Name the blood parasite species.
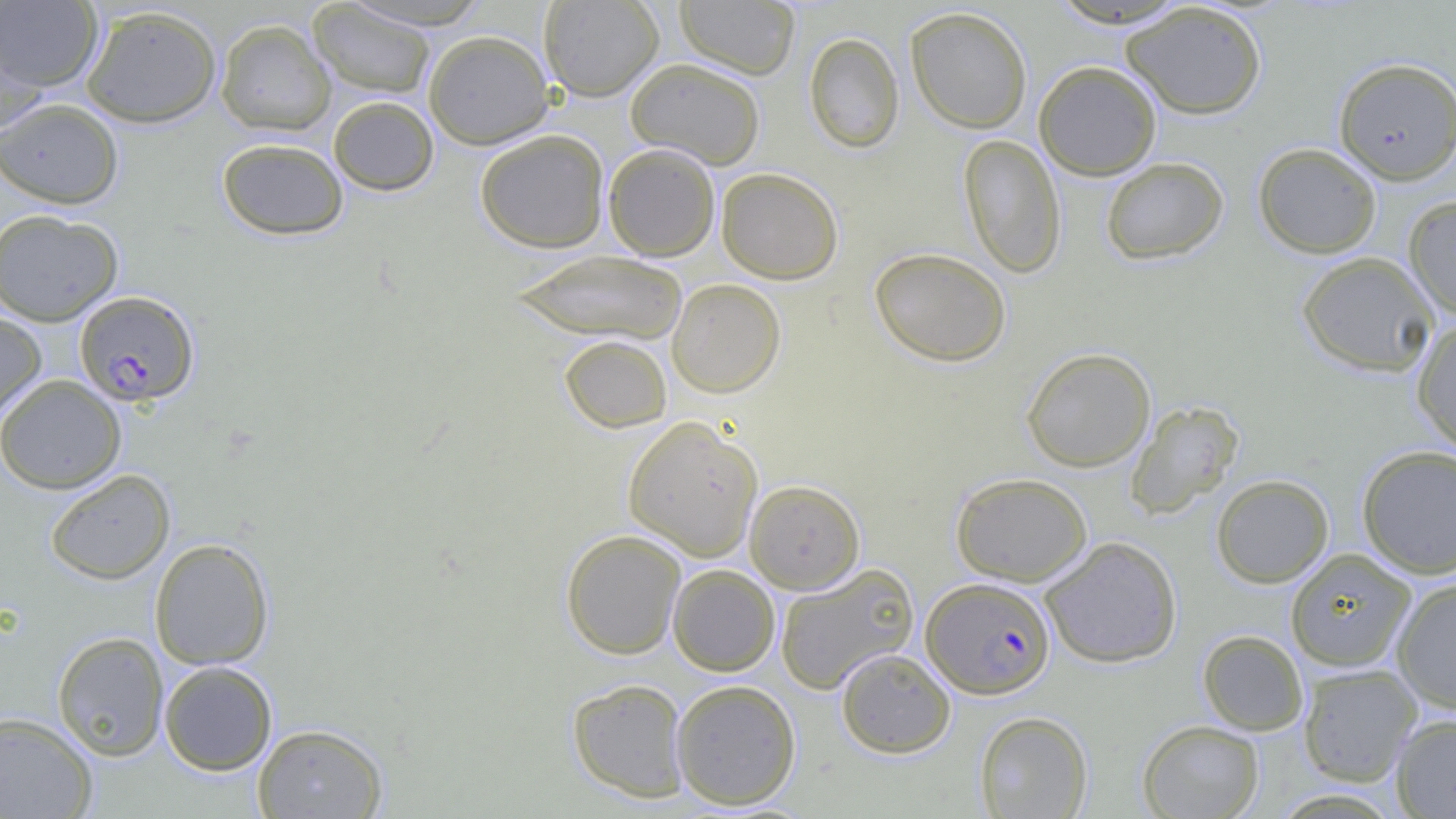

Plasmodium falciparum.

Approximate bounding boxes as (x1, y1, x2, y2) in pixels. Uninfected red blood cell locations: (0, 0, 103, 93), (341, 0, 494, 30), (538, 0, 664, 102), (675, 0, 800, 79), (1045, 1, 1194, 29), (307, 2, 436, 99), (1122, 2, 1267, 120), (80, 4, 222, 128), (905, 6, 1033, 134), (215, 18, 336, 136), (0, 28, 49, 140), (423, 29, 554, 149), (804, 32, 905, 153), (1333, 57, 1456, 184), (625, 58, 766, 170), (1033, 61, 1161, 180), (328, 96, 439, 196), (0, 97, 124, 209), (475, 129, 610, 253), (958, 133, 1066, 279), (216, 137, 349, 240), (1253, 142, 1382, 258), (603, 143, 720, 261), (1100, 157, 1229, 265), (716, 167, 844, 284), (1403, 194, 1456, 322), (0, 208, 123, 326), (869, 247, 1011, 367), (511, 249, 689, 344), (1296, 251, 1440, 376), (667, 278, 786, 398), (0, 309, 47, 424), (1412, 318, 1456, 455), (559, 335, 672, 433), (1021, 347, 1156, 472), (0, 374, 127, 494), (1125, 400, 1244, 519), (623, 415, 763, 561), (1357, 444, 1456, 579), (46, 468, 175, 584), (951, 472, 1093, 586), (1211, 474, 1333, 588), (744, 479, 865, 594), (560, 528, 686, 660), (1040, 536, 1182, 668), (149, 537, 275, 670), (1285, 548, 1416, 672), (774, 563, 919, 694), (667, 564, 780, 676), (1392, 577, 1456, 714), (1198, 629, 1308, 736), (52, 631, 169, 761), (835, 648, 955, 758), (158, 660, 278, 776), (1298, 664, 1422, 786), (567, 678, 690, 802), (670, 679, 801, 809), (0, 710, 98, 819), (974, 711, 1093, 818), (1391, 713, 1456, 818), (1137, 719, 1264, 819), (252, 723, 388, 819). Plasmodium falciparum-infected red blood cell locations: (74, 290, 200, 406), (922, 576, 1056, 699). Optical microscopy. Image is 1456×819 pixels. One field of a larger specimen. Thin blood film. Captured at 1000x magnification.